State which parasite is depicted.
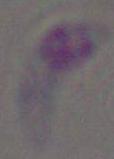

Toxoplasma gondii.

Summary:
  - Modality: photomicrograph
  - Magnification: 1000x